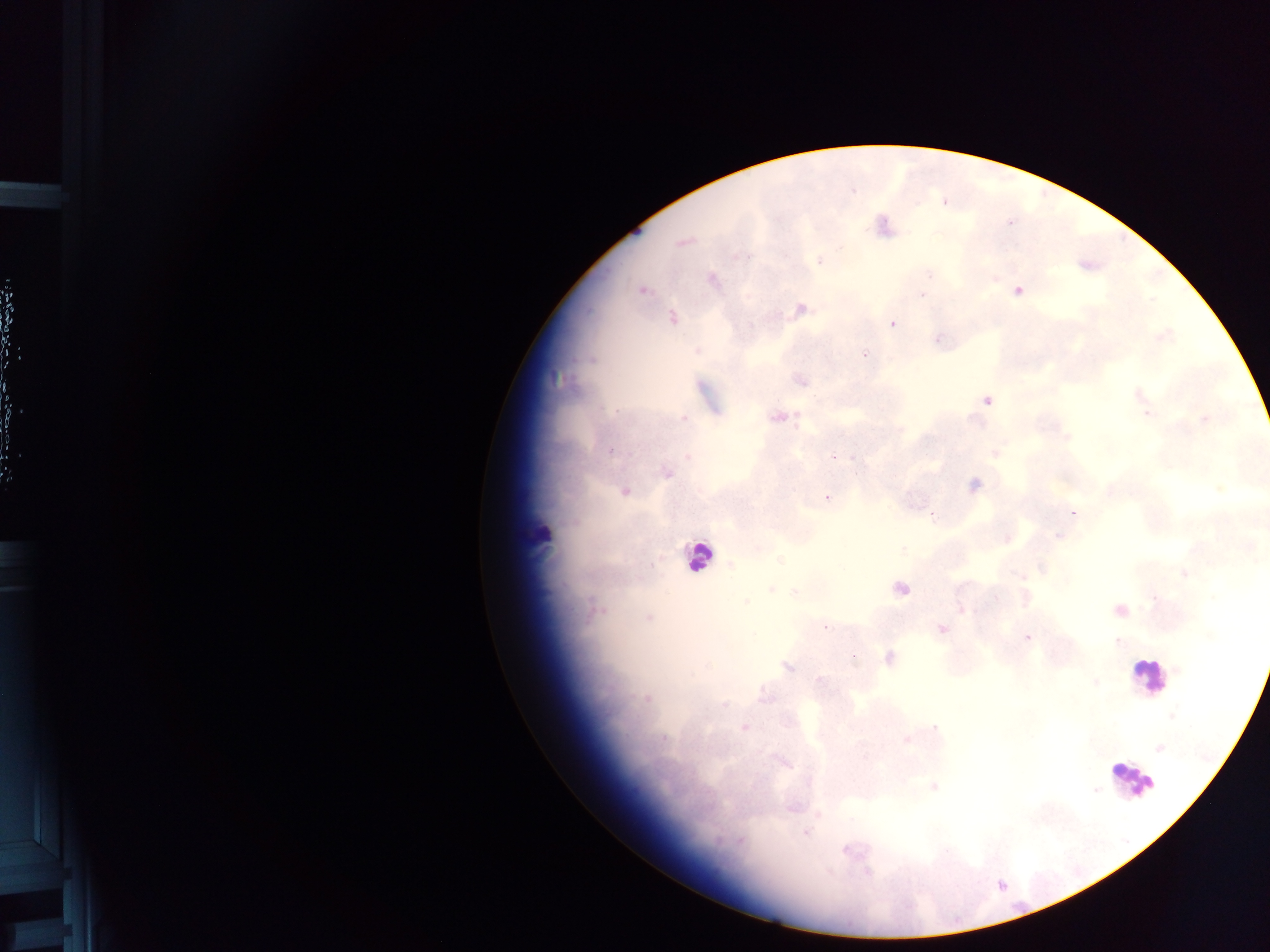
Approximate centers as [x, y] in pixels.
Summary:
  - Object labeled both malaria parasite and leukocyte by the source: [541, 534]
  - Malaria parasite locations: [944, 202], [883, 227], [682, 242], [819, 260], [711, 279], [642, 289], [1018, 290], [922, 296], [799, 310], [671, 318], [893, 323], [1162, 336], [940, 339], [865, 353], [801, 381], [1138, 393], [986, 400], [1146, 413], [779, 416], [684, 418], [1204, 419], [1066, 438], [610, 449], [994, 453], [687, 456], [832, 456], [666, 471], [973, 486], [624, 491], [828, 496], [1073, 513], [1057, 534], [1005, 538], [730, 566], [1184, 574], [1021, 576], [901, 588], [770, 589], [795, 591], [995, 597], [596, 609], [1119, 610], [648, 617], [941, 629], [1026, 638], [888, 658], [787, 666], [819, 680], [647, 697], [743, 727], [907, 739], [1160, 747], [933, 786], [806, 832], [849, 849]
  - Leukocyte locations: [697, 557], [1149, 676], [1132, 779]
  - Country: Ghana
  - Field of view: single
  - Capture: mobile-phone photograph through a microscope
  - Preparation: thick blood film
  - Image size: 1270×952 pixels